Give a bounding box for every artifact (stain precipitate or debris).
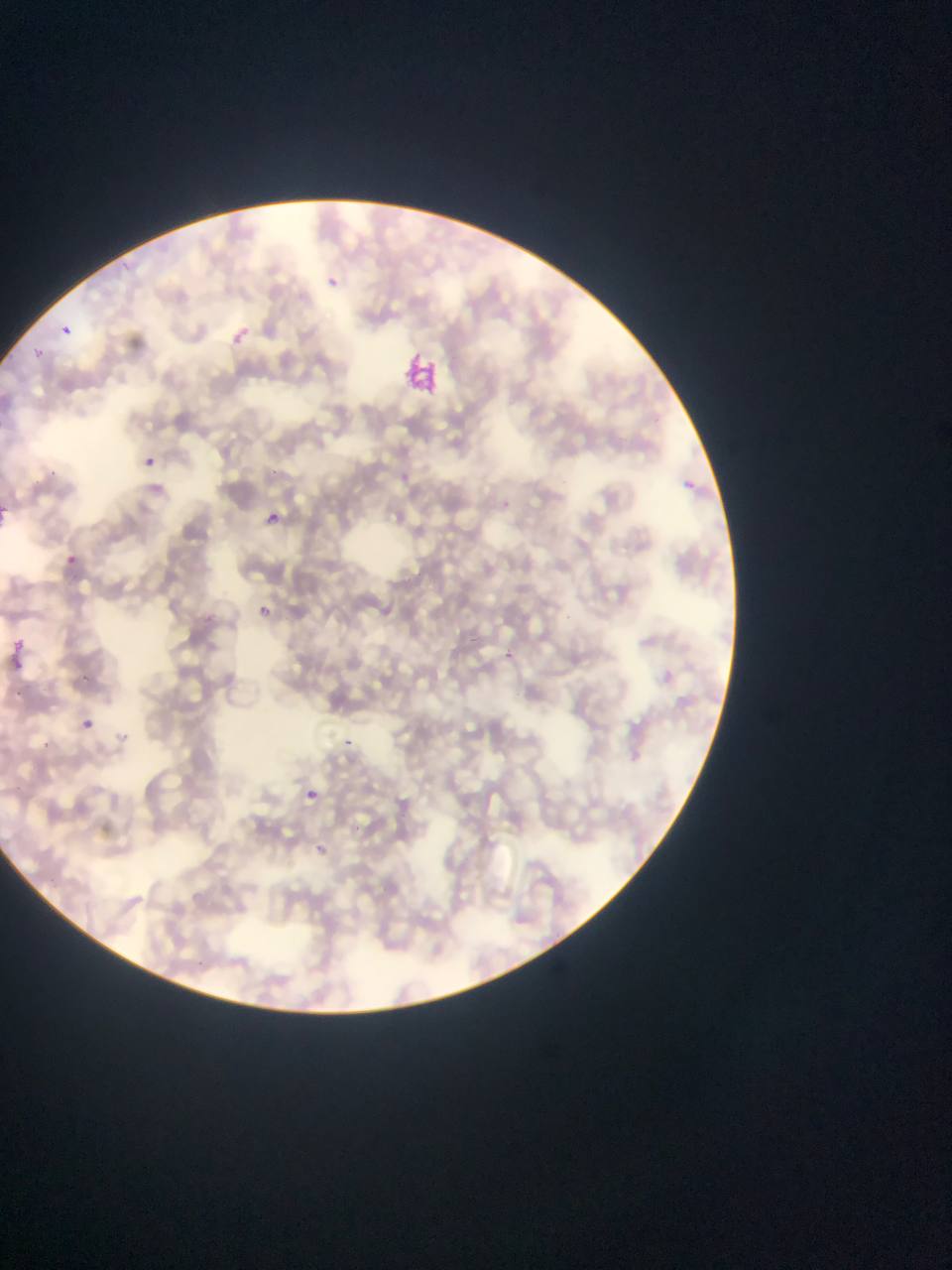

Approximate bounding boxes as (left, top, right, bottom) in pixels.
Artifacts (stain precipitate or debris): (398, 349, 448, 405).

image size = 952×1270 pixels
field of view = single
country = Ghana
capture = mobile-phone photograph through a microscope
preparation = thin blood smear
Plasmodium parasite locations = approximate bounding boxes as (left, top, right, bottom) in pixels: (266, 508, 286, 530), (61, 546, 86, 563), (2, 636, 29, 672)